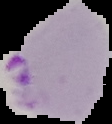
{
  "malaria_status": "parasitized",
  "preparation": "thin blood smear",
  "image_size": "112×124 pixels",
  "image_type": "segmented cell region on a black background"
}